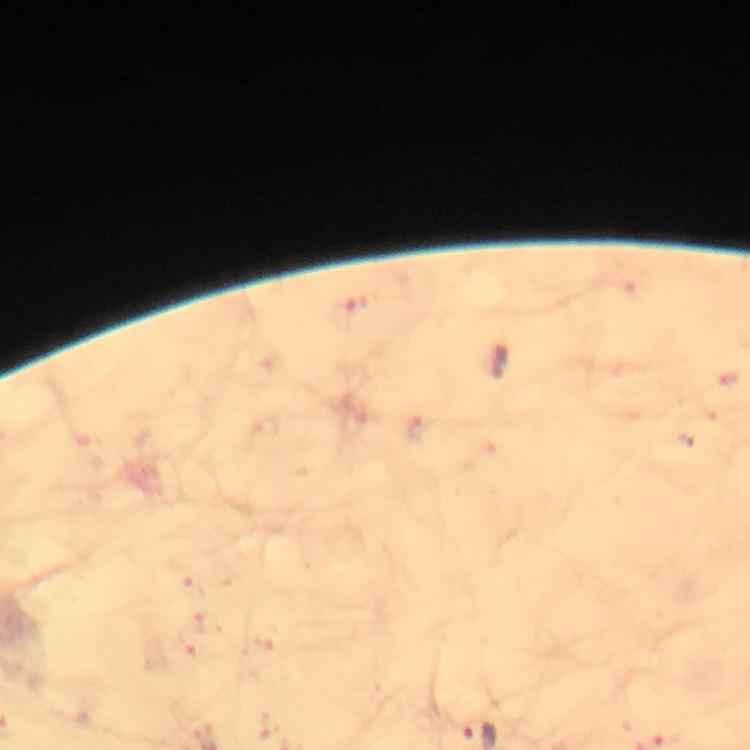 Approximate centers as [x, y] in pixels. Malaria parasite locations: [343, 313]. Thick blood film. Photographed through the microscope with a smartphone camera. 100x magnification. A crop from one field of view. Image is 750×750 pixels. Immersion oil applied. From a diagnostic examination for malaria. Giemsa stain.